Point out every Plasmodium parasite.
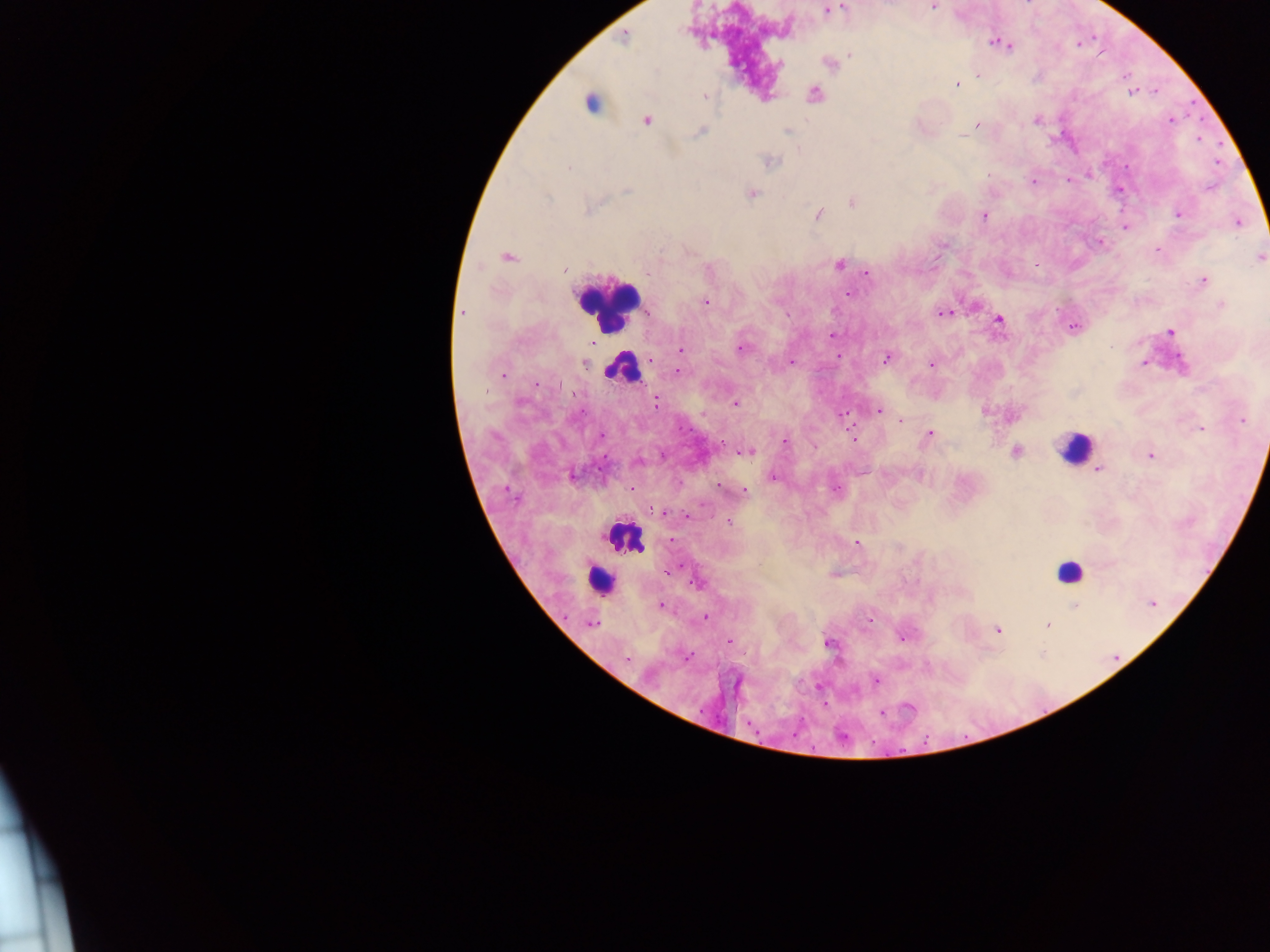
Approximate centers as x y in pixels.
Plasmodium parasites: 932 7; 828 11; 624 38; 998 43; 1007 46; 851 55; 830 65; 978 75; 956 84; 1132 93; 814 94; 705 96; 647 120; 1035 120; 1170 120; 977 125; 788 131; 700 132; 963 135; 772 162; 569 167; 1033 182; 627 191; 751 194; 547 198; 852 202; 592 208; 819 214; 1179 214; 984 216; 1239 223; 1125 227; 1157 250; 507 257; 1259 258; 840 264; 1036 264; 564 270; 867 274; 1204 280; 849 294; 704 302; 1221 304; 463 312; 944 313; 999 319; 1073 327; 1171 332; 831 335; 741 348; 681 350; 838 356; 885 359; 791 362; 1144 363; 1182 363; 584 364; 930 365; 677 371; 502 374; 656 403; 735 403; 879 411; 843 416; 1242 420; 900 421; 1200 428; 929 434; 852 437; 785 442; 749 452; 1015 452; 1151 456; 638 461; 1098 469; 573 476; 773 477; 744 492; 655 514; 729 524; 857 543; 698 583; 1153 603; 1075 605; 661 606; 706 618; 592 624; 1047 625; 998 629; 902 637; 730 641; 828 642; 627 659; 876 680.

Leukocyte locations: 590 102; 608 305; 622 369; 1074 447; 628 536; 1069 571; 596 579. Thick blood film. Photographed through a microscope with a mobile-phone camera. One field of view. Sample from Ghana. Image is 1270×952 pixels.